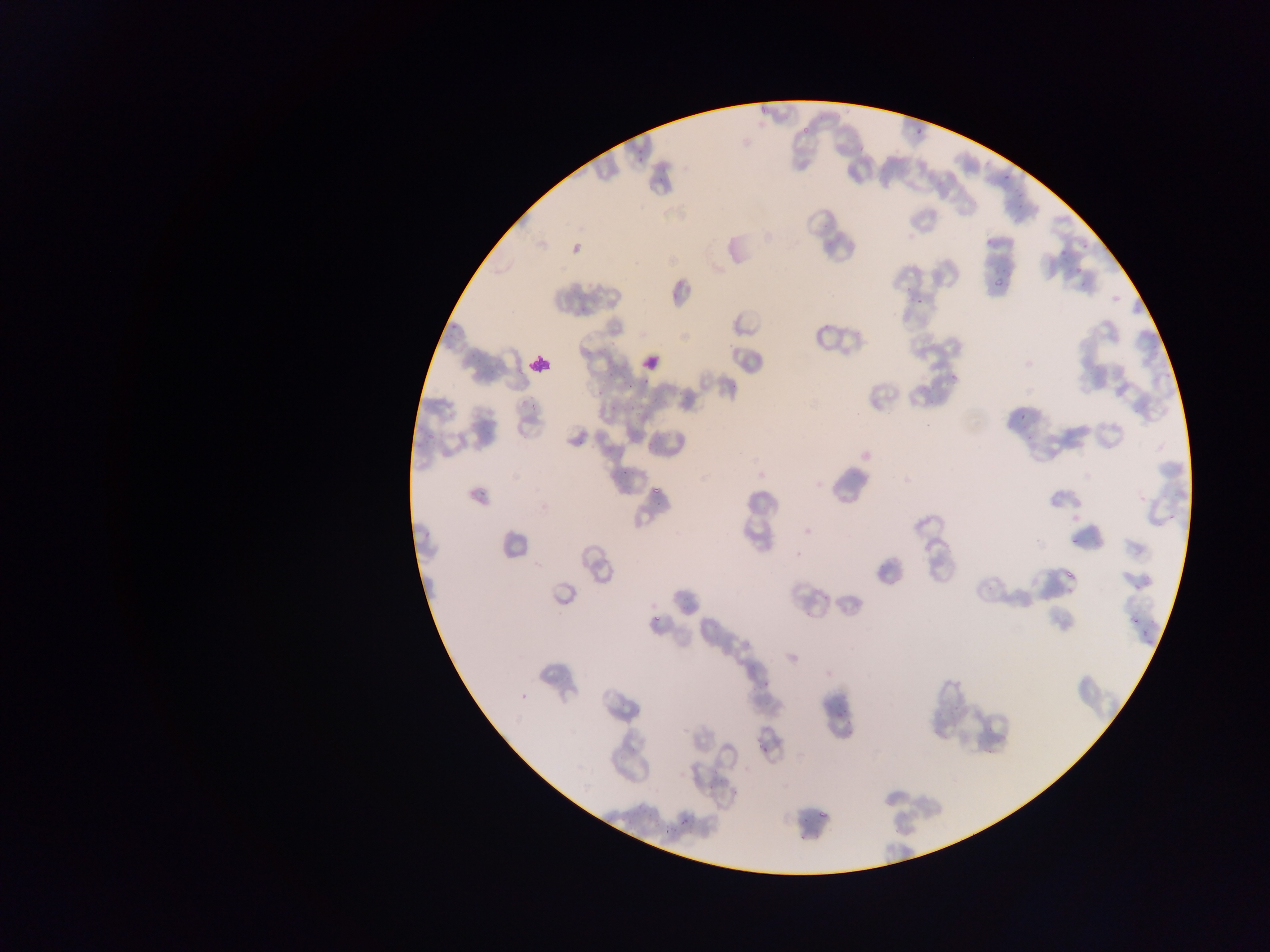
Approximate bounding boxes as (left, top, right, bottom) in pixels. Leukocyte locations: (638, 351, 663, 374), (529, 353, 552, 375). Plasmodium parasite locations: (758, 105, 771, 117), (801, 126, 810, 137), (915, 127, 922, 135), (634, 149, 641, 162), (1002, 175, 1010, 183), (656, 179, 665, 190), (1058, 242, 1067, 255), (571, 244, 581, 253), (1076, 265, 1085, 272), (989, 278, 1008, 291), (914, 295, 933, 305), (949, 374, 957, 382), (635, 378, 654, 386), (625, 379, 633, 389), (609, 400, 620, 411), (630, 400, 641, 415), (1019, 407, 1027, 420), (618, 473, 628, 478), (652, 487, 660, 495), (1170, 511, 1179, 518), (1062, 559, 1087, 581), (1133, 579, 1144, 594), (651, 616, 661, 626), (1126, 617, 1137, 627), (1138, 622, 1149, 635), (1144, 640, 1152, 650), (835, 693, 851, 712), (758, 741, 768, 756), (820, 804, 831, 819), (797, 812, 808, 822), (670, 814, 689, 825), (665, 826, 674, 835) | approximate (x, y) pixel centers of objects too small to bound: (600, 391). Single field of view. Image is 1270×952 pixels. Thin blood film. Sample from Ghana. Photographed through a microscope with a mobile-phone camera.